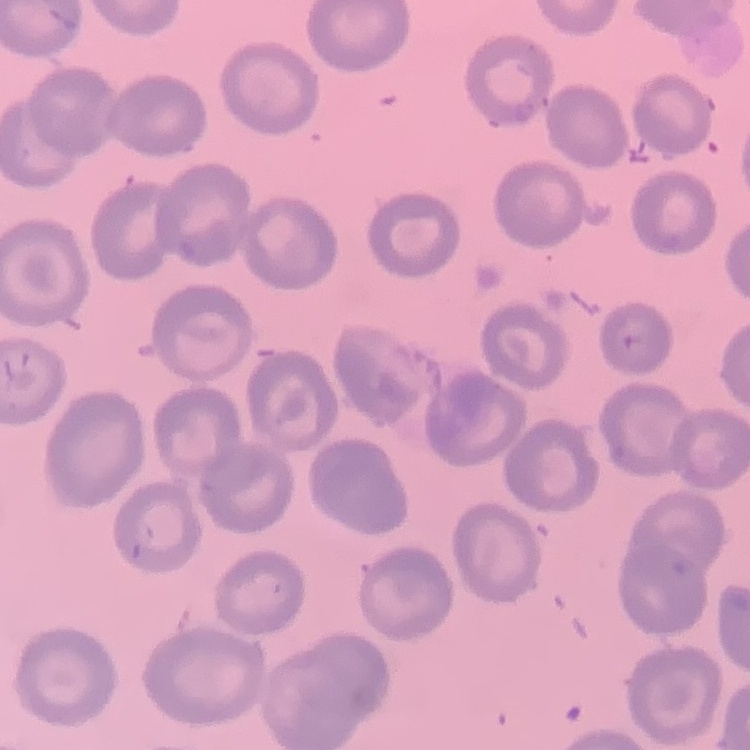
Summary:
  - Erythrocyte morphology: no rouleaux formation
  - Preparation: thin peripheral smear
  - Stain: Field's or Giemsa
  - Image type: square crop of a larger photomicrograph